Assess the morphology of the erythrocytes.
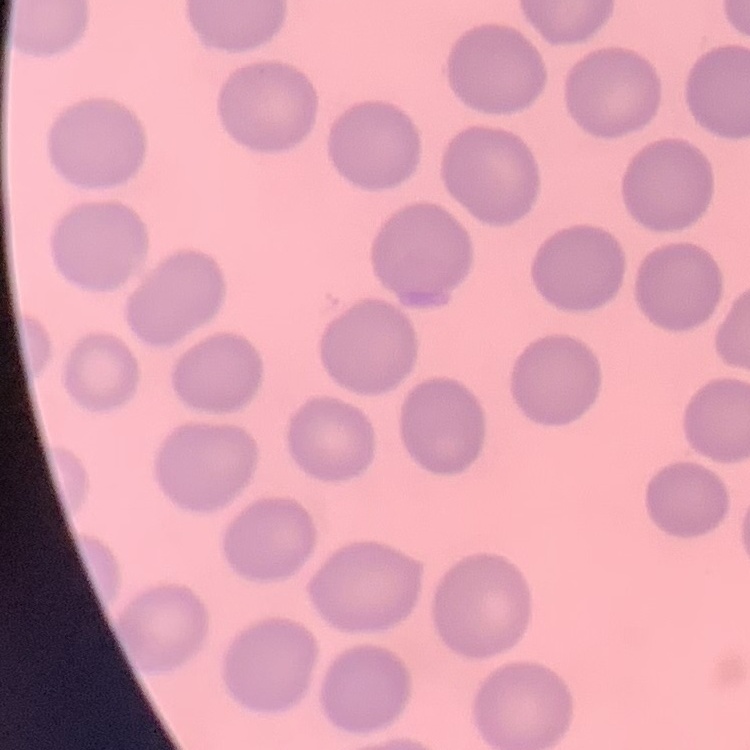
They show no rouleaux formation.

One tile cut from a larger photomicrograph. Field's or Giemsa stain. Thin blood film.